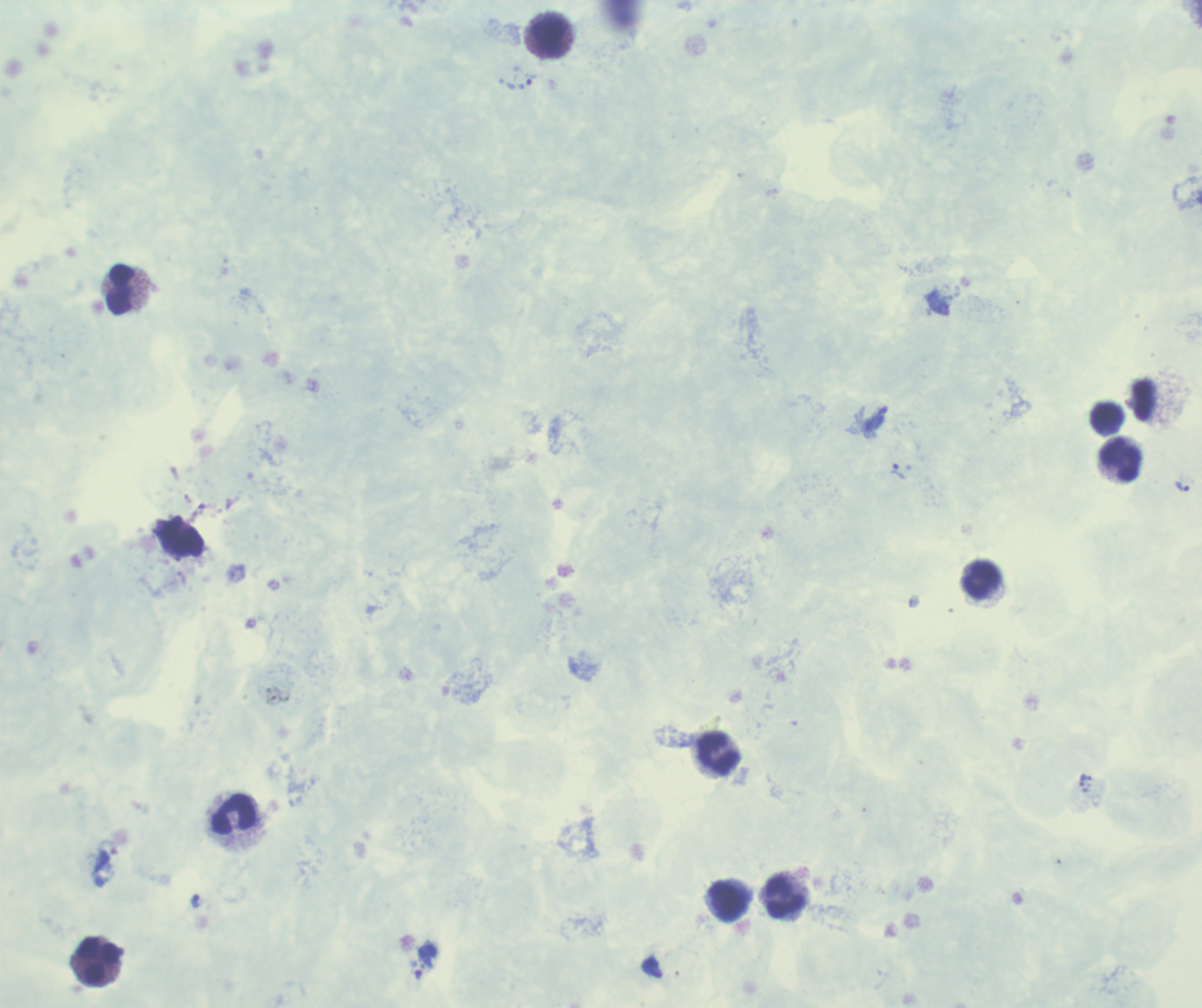
Approximate centers as [x, y] in pixels. Trophozoite locations: [876, 419], [898, 471], [1182, 487], [1083, 781], [426, 960]. Leukocyte locations: [549, 36], [119, 291], [1143, 400], [1107, 419], [1120, 460], [182, 538], [980, 581], [718, 754], [234, 815], [784, 897], [727, 902], [98, 962]. 100x magnification. Previously used in an actual diagnosis. Romanowsky-stained preparation. Result: positive for malaria parasites. Image is 1202×1008 pixels. Background quality: unsatisfactory. Thick smear of blood. One field from this slide.